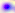
Photomicrograph. Captured at 400x magnification. Toxoplasma gondii is seen.